Identify the parasite.
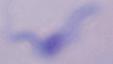
A trypanosome.

Photomicrograph. 1000x magnification.